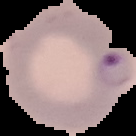
Summary:
  - Image size: 136×136 pixels
  - Result: Plasmodium parasites identified
  - Preparation: thin blood smear
  - Image type: cell region segmented out of the field of view; surrounding area masked to black